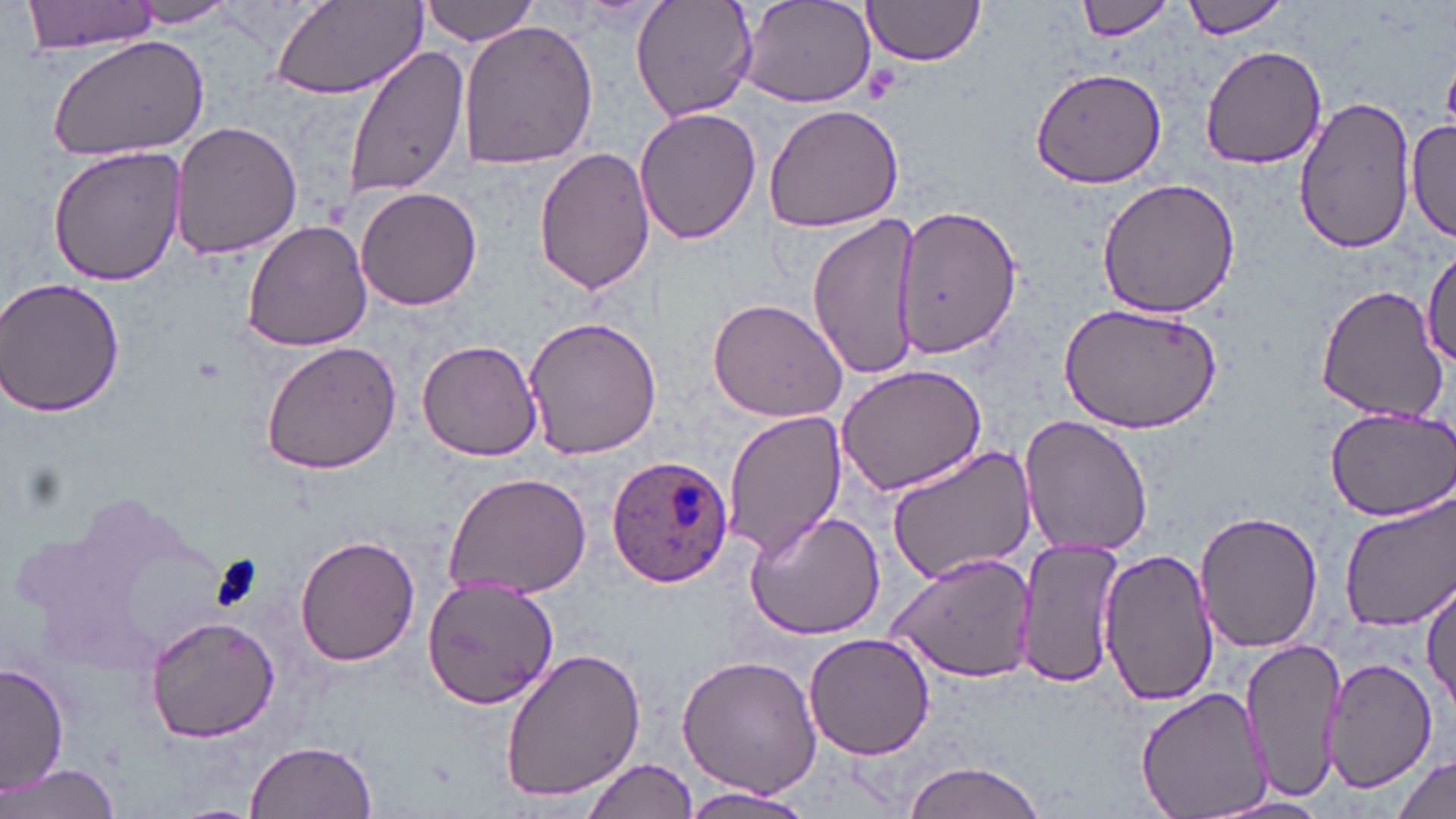 Approximate bounding boxes as (x1, y1, x2, y2) in pixels. Plasmodium ovale-infected red blood cell locations: (606, 454, 734, 587). Uninfected red blood cell locations: (23, 0, 160, 53), (269, 0, 427, 101), (421, 0, 542, 47), (629, 0, 758, 123), (737, 0, 878, 110), (861, 0, 987, 66), (1074, 0, 1179, 42), (1181, 0, 1290, 37), (120, 1, 241, 28), (458, 19, 598, 171), (45, 33, 211, 162), (342, 43, 469, 202), (1199, 45, 1327, 170), (1029, 64, 1167, 189), (1293, 96, 1416, 255), (762, 101, 906, 232), (634, 107, 762, 246), (1408, 117, 1455, 240), (169, 120, 303, 261), (47, 144, 187, 287), (534, 145, 654, 295), (1097, 176, 1242, 320), (355, 186, 482, 312), (891, 209, 1021, 359), (807, 211, 920, 383), (242, 220, 372, 353), (1421, 247, 1456, 368), (0, 277, 128, 417), (1316, 283, 1447, 421), (706, 295, 847, 425), (1058, 300, 1222, 433), (522, 313, 664, 458), (416, 339, 541, 461), (260, 342, 401, 476), (835, 362, 989, 498), (1323, 402, 1456, 520), (722, 409, 847, 559), (1018, 414, 1153, 559), (884, 446, 1038, 584), (441, 470, 592, 601), (26, 490, 238, 679), (1338, 496, 1456, 633), (743, 509, 886, 640), (1194, 509, 1323, 654), (294, 534, 420, 668), (1016, 537, 1126, 688), (1098, 548, 1217, 709), (885, 551, 1037, 682), (423, 577, 559, 710), (1422, 578, 1456, 710), (142, 612, 285, 743), (802, 633, 934, 760), (1241, 636, 1347, 803), (500, 646, 647, 804), (675, 655, 823, 799), (1325, 656, 1436, 789), (2, 664, 70, 794), (1133, 686, 1276, 819), (245, 739, 377, 819), (1389, 753, 1453, 819), (579, 758, 695, 819), (897, 760, 1049, 819), (3, 761, 122, 818), (679, 785, 814, 818), (1202, 794, 1339, 819). Platelet locations: (864, 68, 901, 105), (206, 553, 263, 616). Slide-level diagnosis: Plasmodium ovale. Captured at 1000x magnification. May-Grünwald-Giemsa-stained preparation. Optical microscopy. One field of a larger specimen. Thin blood smear. Image is 1456×819 pixels.